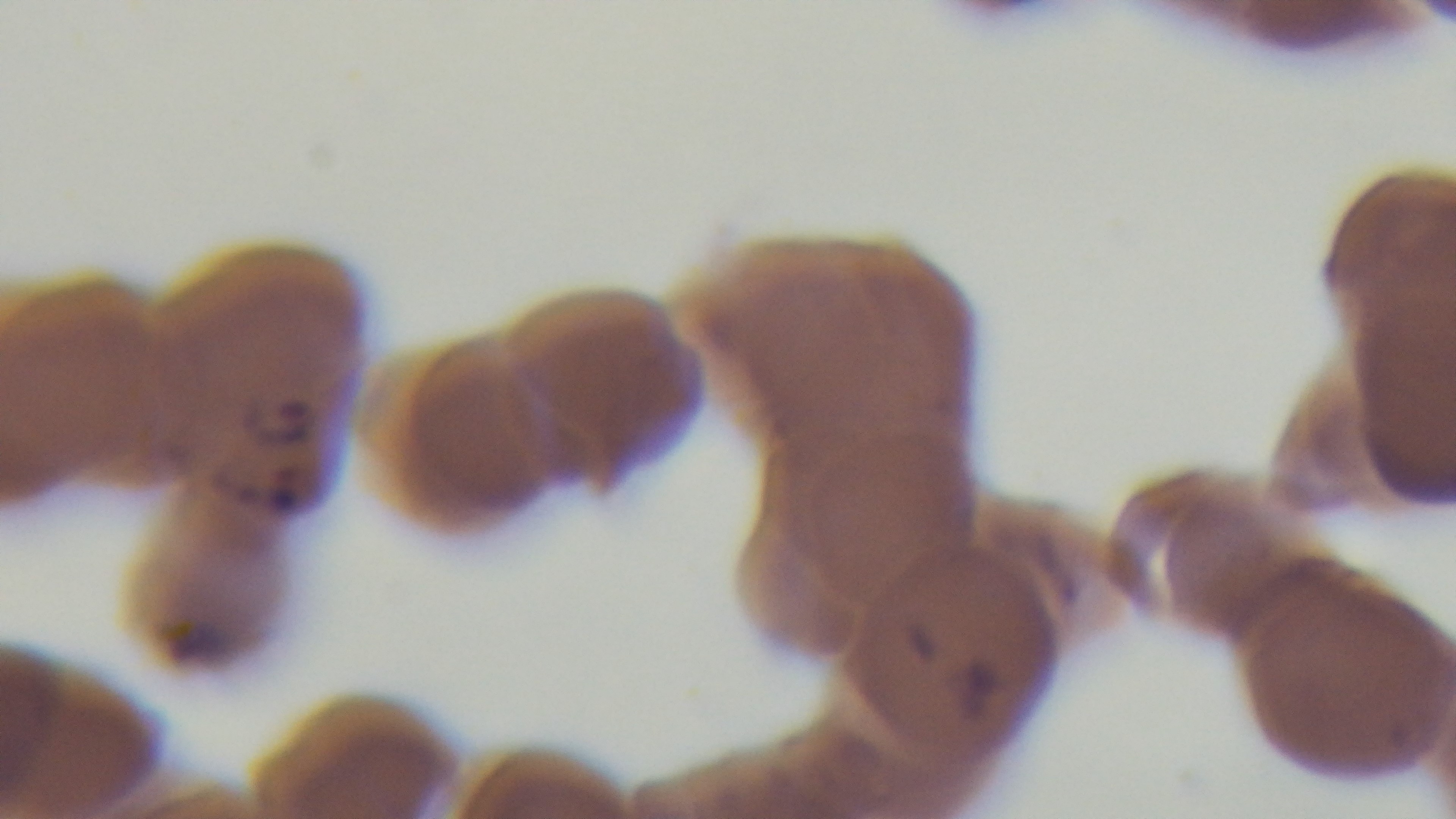 Light microscopy. Single field of view. Captured with a mounted 4K digital camera. Malaria status: infected. Preparation: thin. Oil-immersion objective, 100x. Giemsa stain.